Classify this cell by malaria status.
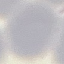

Uninfected.

capture = smartphone camera at the microscope eyepiece
preparation = thin blood smear
image type = cell patch, automatically extracted from a larger field of view and resized to 64 × 64 pixels
stain = Giemsa